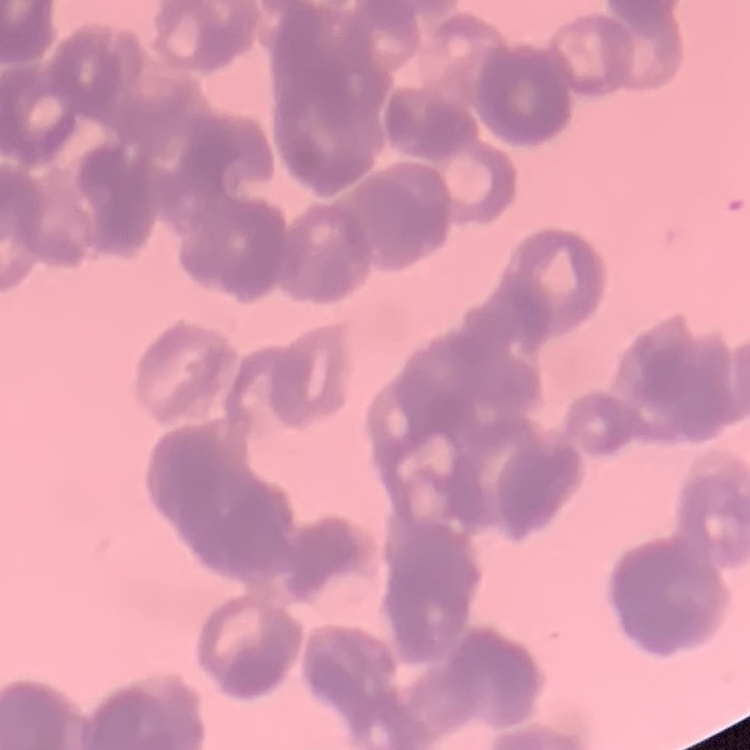
Summary:
  - Red blood cell morphology: rouleaux formation
  - Stain: Field's or Giemsa
  - Preparation: thin peripheral smear
  - Image type: one tile cut from a larger photomicrograph